Report the malaria status of this cell.
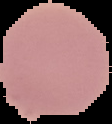

It is uninfected.

image type = segmented cell region on a black background
image size = 112×124 pixels
preparation = thin blood film